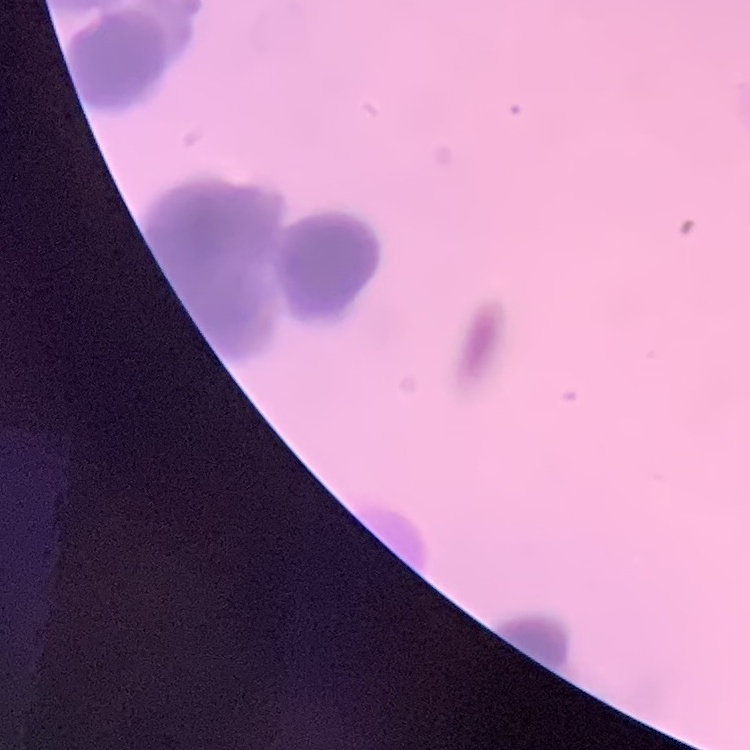

Summary:
  - Red blood cell morphology: rouleaux formation
  - Image type: square crop of a larger photomicrograph
  - Preparation: thin peripheral smear
  - Stain: Field's or Giemsa